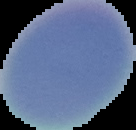

From a thin blood smear. Segmented cell region on a black background. Result: no malaria parasites detected. Image is 136×130 pixels.